Assess this cell for malaria.
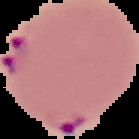
It is parasitized.

Summary:
  - Preparation: thin blood film
  - Image type: segmented cell region on a black background
  - Image size: 139×139 pixels